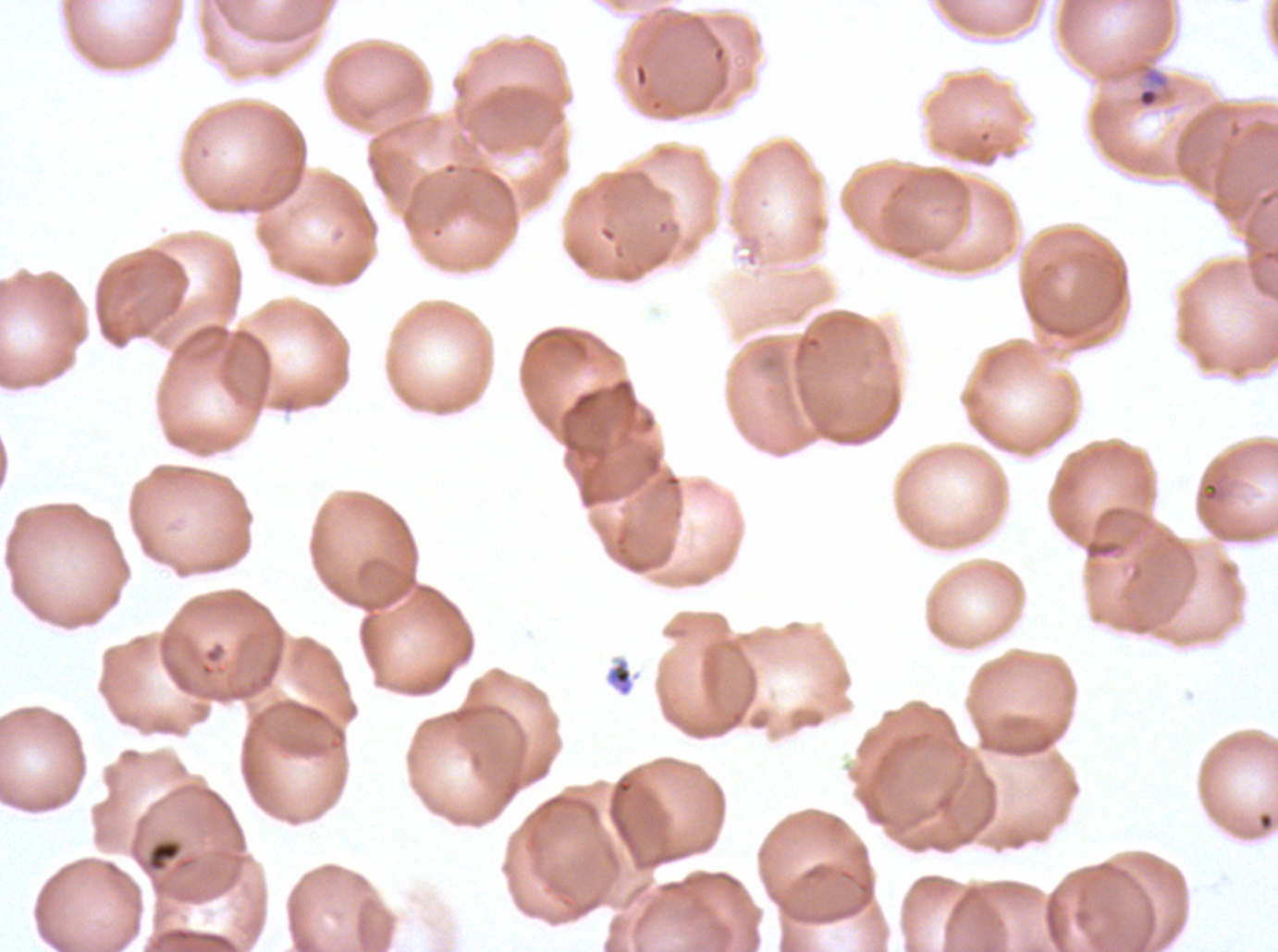
Approximate bounding rectangles given as corner coordinates in pixels from the top-left.
Summary:
  - Late-ring/early-trophozoite locations: (x1=1136, y1=66, x2=1170, y2=110)
  - Debris locations: (x1=605, y1=657, x2=635, y2=697), (x1=146, y1=838, x2=183, y2=873)
  - Field of view: sub-image separated from a larger composite
  - Stain: Giemsa
  - Specimen: ex-vivo Plasmodium falciparum culture from a patient in The Gambia, grown for 24 to 48 hours
  - Preparation: thin blood smear
  - Image size: 1278×952 pixels